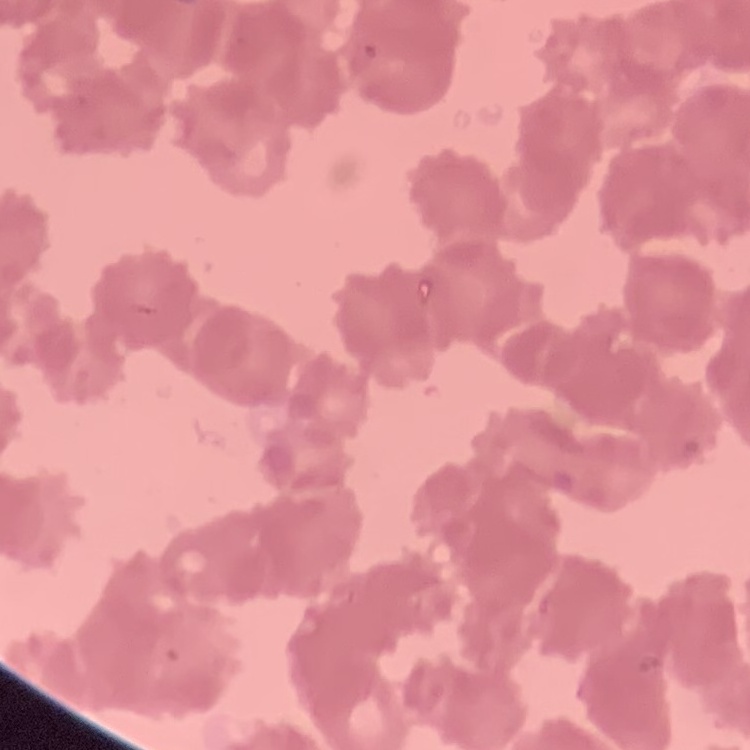

Summary:
  - Erythrocyte morphology: rouleaux formation
  - Preparation: thin blood film
  - Stain: Field's or Giemsa
  - Image type: one tile cut from a larger photomicrograph